Classify this cell by malaria status.
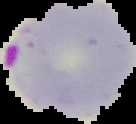
It is parasitized.

image size = 136×124 pixels
image type = segmented cell region with the area outside set to black
preparation = thin blood smear